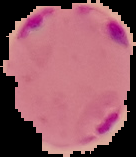 The area outside the segmented cell region is set to black. Result: Plasmodium parasites detected. Image is 136×157 pixels. From a thin blood film.